Report the malaria status of this cell.
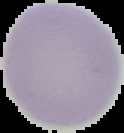
It is uninfected.

The area outside the segmented cell region is set to black. From a thin blood film. Image is 124×133 pixels.